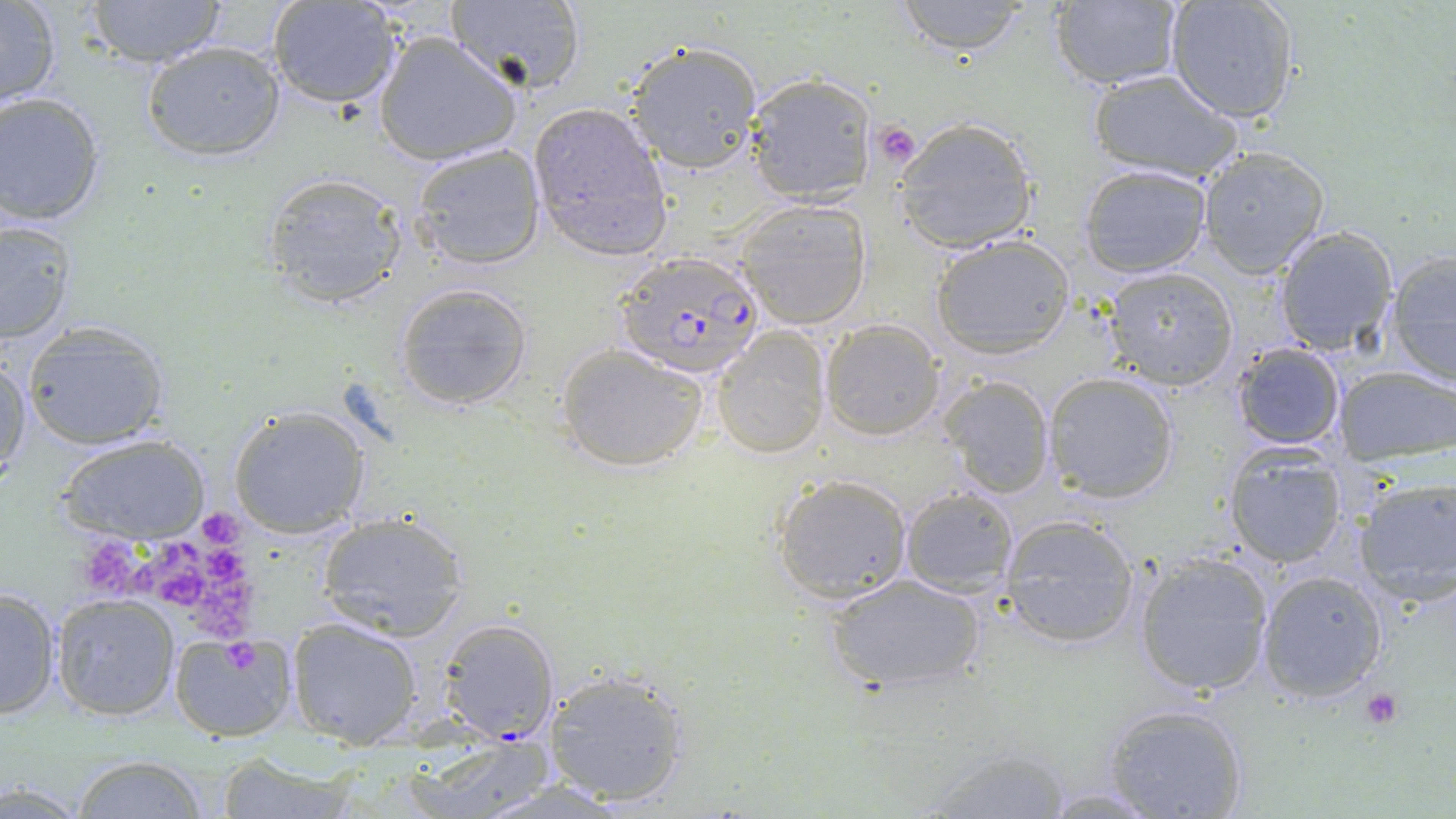

Summary:
  - Coordinate format: approximate bounding boxes as (x1, y1, x2, y2) in pixels
  - Platelet locations: (872, 120, 920, 166), (200, 511, 244, 550), (149, 533, 197, 572), (87, 542, 139, 601), (208, 547, 245, 585), (158, 569, 204, 609), (202, 582, 256, 637), (228, 636, 259, 668), (1361, 688, 1402, 728)
  - Uninfected red blood cell locations: (86, 0, 227, 66), (445, 0, 588, 97), (893, 0, 1032, 54), (1164, 0, 1301, 123), (0, 2, 63, 106), (266, 2, 403, 110), (1048, 2, 1183, 89), (375, 33, 523, 167), (139, 41, 286, 161), (625, 41, 764, 173), (1088, 68, 1245, 183), (741, 72, 877, 203), (0, 92, 105, 226), (526, 101, 674, 263), (893, 117, 1040, 254), (409, 142, 547, 271), (1196, 147, 1330, 278), (1076, 164, 1213, 279), (261, 171, 410, 309), (735, 199, 871, 329), (1, 217, 77, 348), (1272, 223, 1399, 358), (930, 235, 1075, 357), (1385, 248, 1456, 387), (1102, 266, 1239, 391), (393, 283, 531, 410), (820, 319, 946, 441), (20, 321, 171, 453), (711, 327, 830, 459), (1229, 343, 1347, 450), (557, 345, 708, 473), (1, 358, 32, 487), (1332, 367, 1456, 463), (1042, 370, 1181, 501), (940, 375, 1055, 498), (228, 406, 372, 537), (59, 434, 210, 544), (1221, 443, 1350, 568), (772, 473, 913, 605), (1351, 475, 1455, 603), (898, 485, 1018, 597), (315, 512, 468, 642), (998, 514, 1141, 648), (1133, 550, 1274, 698), (1256, 568, 1388, 701), (823, 572, 989, 697), (0, 586, 61, 722), (50, 594, 181, 722), (436, 617, 560, 743), (285, 618, 424, 747), (166, 631, 299, 743), (543, 670, 692, 806), (1103, 702, 1249, 819), (397, 740, 565, 819), (916, 748, 1077, 818), (68, 753, 211, 818), (210, 756, 365, 818), (1, 778, 90, 815)
  - Plasmodium falciparum-infected red blood cell locations: (612, 251, 768, 377)
  - Slide-level diagnosis: Plasmodium falciparum
  - Preparation: thin blood smear
  - Field of view: single
  - Image size: 1456×819 pixels
  - Modality: light microscopy
  - Stain: May-Grünwald-Giemsa
  - Magnification: 1000x